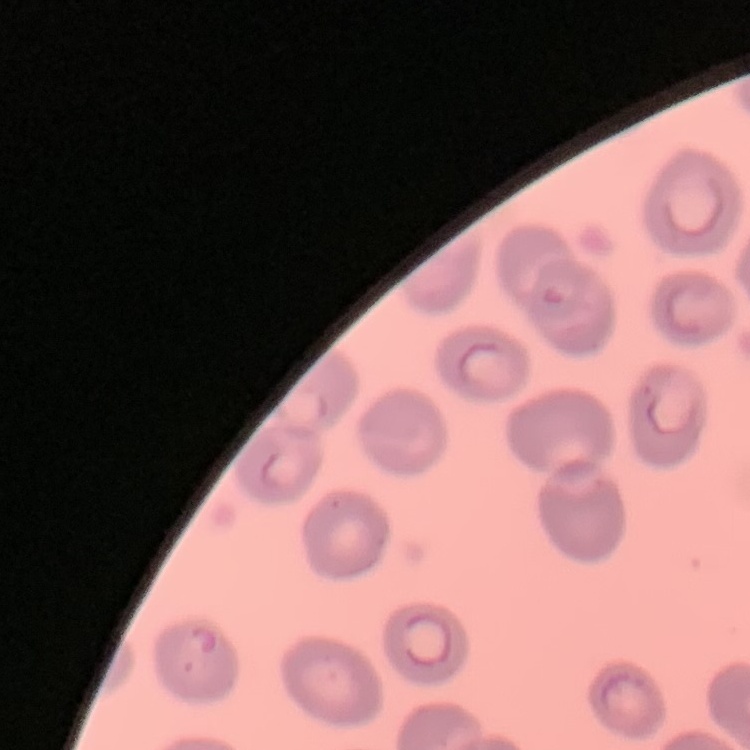

red blood cell morphology = no rouleaux formation
stain = Field's or Giemsa
preparation = thin blood film
image type = square crop of a larger photomicrograph